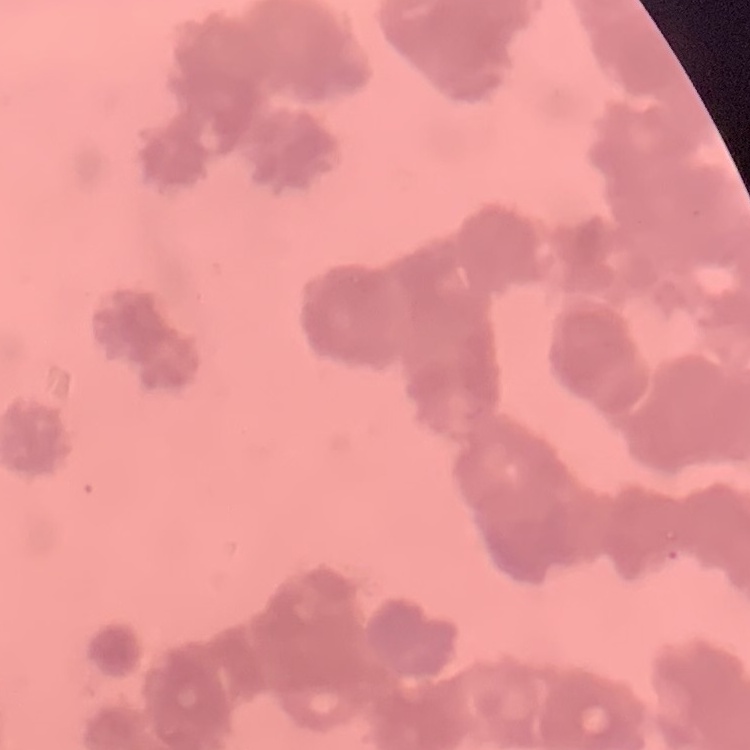
Summary:
  - Red blood cell morphology: rouleaux formation
  - Stain: Field's or Giemsa
  - Preparation: thin peripheral smear
  - Image type: square crop of a larger photomicrograph